Name the blood parasite species.
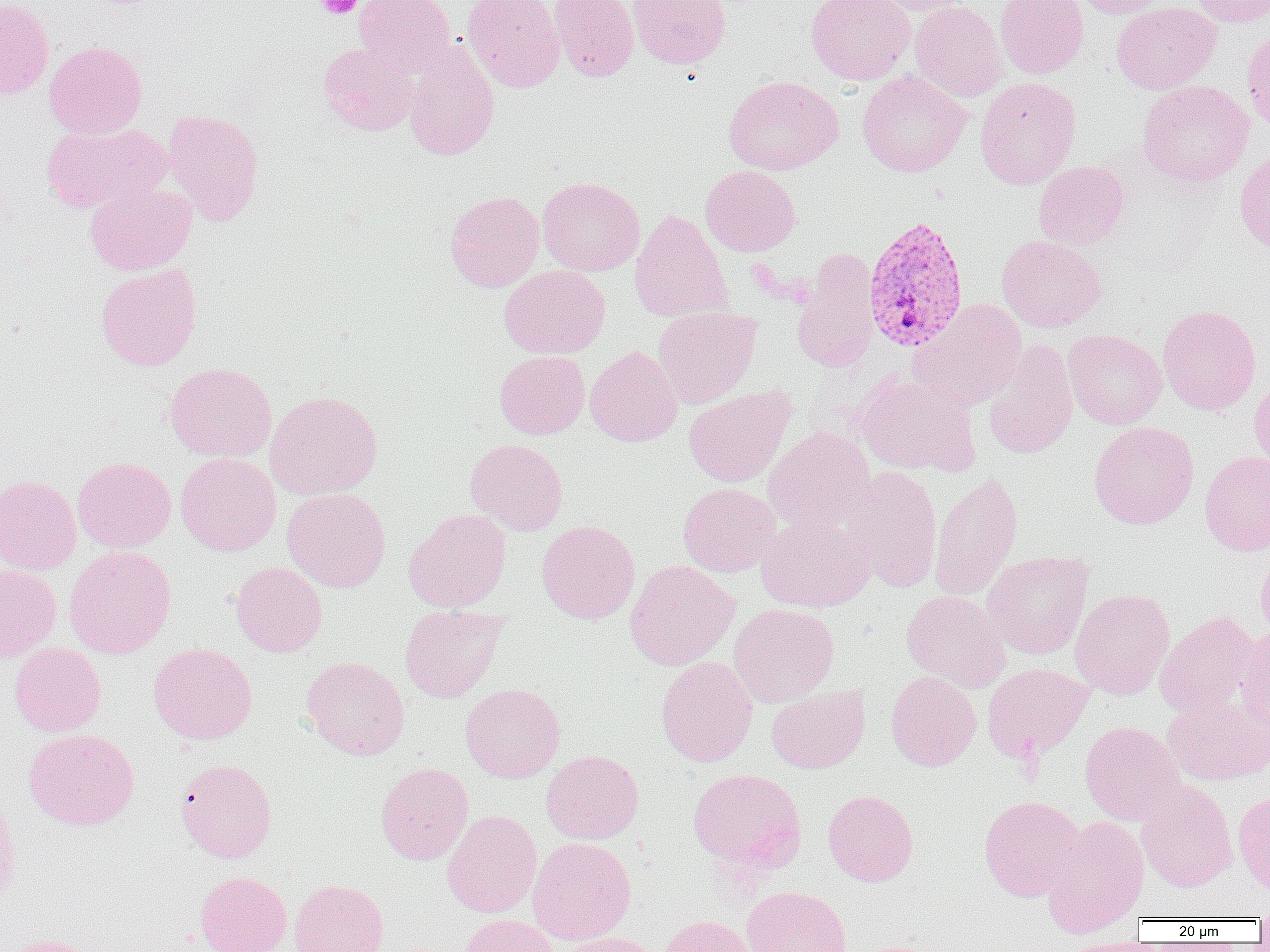
Plasmodium vivax.

Summary:
  - Coordinate format: approximate bounding boxes as (x1, y1, x2, y2) in pixels
  - Platelet locations: (315, 0, 363, 19)
  - Uninfected red blood cell locations: (0, 0, 54, 100), (354, 0, 454, 78), (463, 0, 564, 92), (549, 0, 639, 82), (629, 0, 730, 69), (806, 0, 915, 85), (870, 0, 975, 15), (995, 0, 1089, 79), (1071, 0, 1171, 18), (1189, 0, 1270, 27), (910, 1, 1008, 102), (1112, 3, 1221, 94), (1241, 28, 1270, 131), (44, 40, 147, 139), (403, 40, 500, 161), (318, 42, 418, 136), (857, 71, 971, 177), (723, 76, 842, 175), (975, 77, 1081, 189), (1137, 80, 1254, 186), (163, 109, 264, 225), (40, 123, 169, 214), (1235, 148, 1270, 254), (1033, 161, 1129, 250), (700, 165, 801, 256), (537, 177, 644, 276), (84, 181, 196, 276), (444, 190, 544, 292), (630, 209, 731, 322), (996, 235, 1107, 332), (791, 250, 880, 372), (96, 265, 202, 370), (499, 265, 610, 358), (909, 299, 1028, 411), (1158, 304, 1261, 415), (653, 308, 761, 409), (1063, 329, 1167, 430), (982, 339, 1078, 460), (585, 346, 683, 446), (495, 351, 589, 439), (165, 362, 277, 462), (853, 370, 979, 477), (851, 372, 961, 591), (1250, 376, 1270, 473), (683, 385, 796, 488), (265, 391, 383, 500), (1089, 421, 1199, 529), (763, 426, 876, 533), (465, 438, 568, 536), (1199, 451, 1270, 555), (176, 452, 281, 556), (73, 456, 176, 553), (840, 466, 943, 592), (929, 471, 1024, 602), (0, 474, 81, 575), (678, 483, 781, 577), (282, 488, 391, 592), (404, 509, 511, 612), (756, 512, 876, 612), (537, 520, 641, 623), (63, 545, 176, 658), (981, 550, 1094, 658), (1256, 550, 1270, 645), (625, 560, 739, 670), (230, 562, 328, 657), (0, 564, 61, 663), (1070, 589, 1174, 700), (901, 590, 1011, 692), (728, 603, 839, 707), (399, 604, 507, 704), (1155, 610, 1261, 717), (1236, 626, 1270, 734), (9, 643, 106, 736), (147, 643, 258, 744), (301, 656, 410, 760), (656, 657, 758, 767), (982, 662, 1092, 763), (886, 670, 981, 771), (460, 683, 565, 783), (766, 685, 870, 774), (1163, 694, 1270, 785), (1079, 720, 1185, 826), (23, 728, 139, 830), (541, 749, 644, 844), (175, 758, 277, 863), (376, 763, 473, 864), (687, 768, 806, 872), (1136, 778, 1238, 892), (1233, 789, 1270, 896), (0, 790, 20, 910), (822, 790, 918, 887), (978, 795, 1085, 902), (442, 810, 542, 918), (1039, 815, 1149, 937), (527, 837, 636, 945), (194, 871, 292, 952), (289, 879, 388, 952), (742, 886, 851, 952), (459, 914, 558, 952), (658, 915, 761, 951), (553, 932, 665, 952), (3, 935, 104, 952), (1054, 937, 1158, 952)
  - Plasmodium vivax-infected red blood cell locations: (863, 214, 970, 352)
  - Modality: optical microscopy
  - Magnification: 1000x
  - Preparation: thin blood film
  - Image size: 1270×952 pixels
  - Field of view: one of a larger specimen